Locate every blood parasite and identify its species.
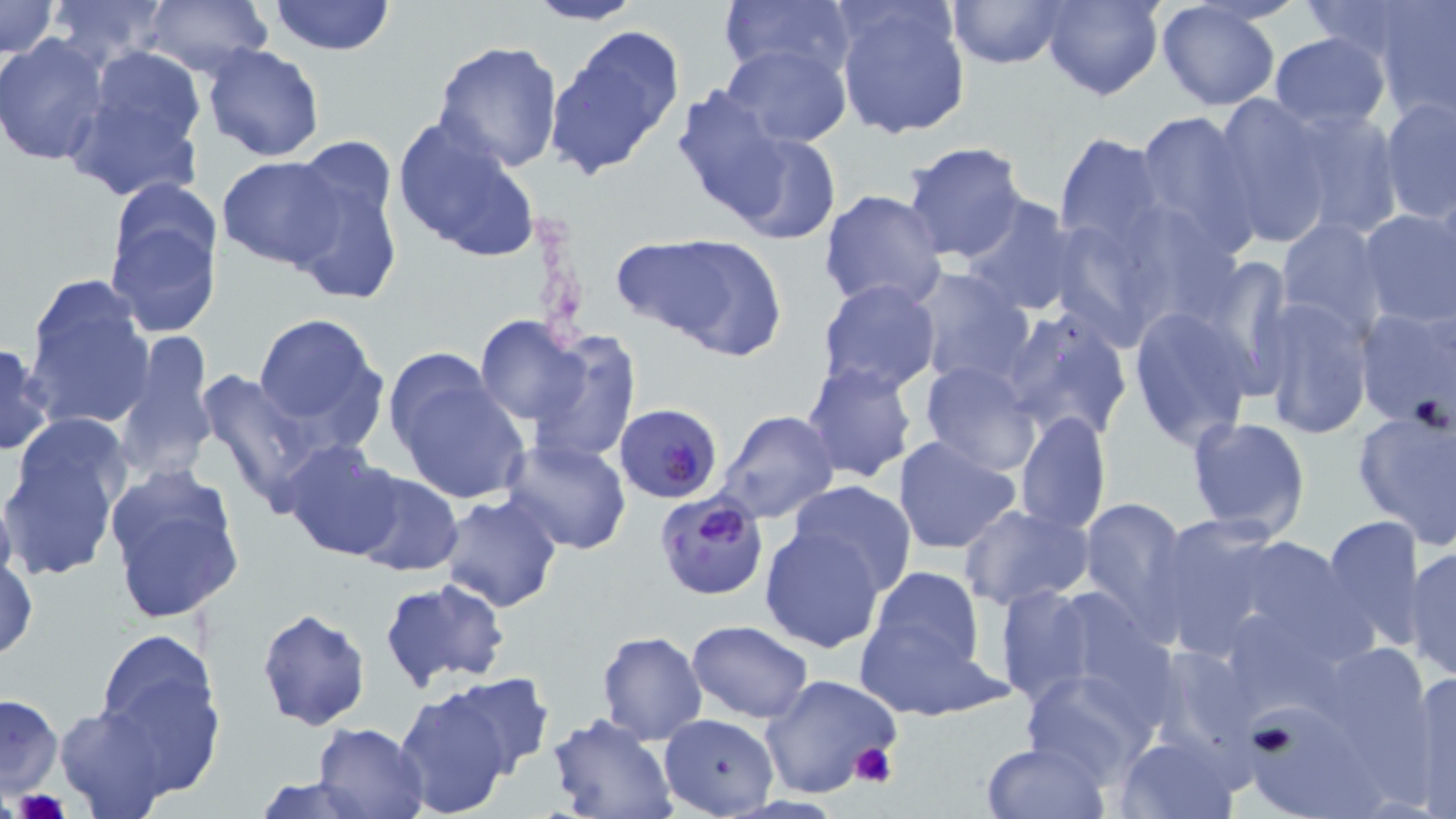
Approximate bounding boxes as (x1, y1, x2, y2) in pixels.
Plasmodium falciparum-infected red blood cells: (615, 403, 723, 503), (653, 491, 768, 600).
No Plasmodium ovale, Plasmodium malariae, Plasmodium vivax, Babesia divergens, or Trypanosoma brucei observed.

Platelet locations: (851, 743, 897, 788), (16, 790, 67, 819). Uninfected red blood cell locations: (0, 0, 59, 58), (41, 0, 176, 68), (142, 0, 273, 81), (267, 0, 397, 56), (525, 0, 642, 25), (718, 0, 856, 88), (946, 0, 1069, 69), (1042, 0, 1162, 101), (831, 1, 970, 141), (1156, 2, 1282, 111), (1374, 2, 1456, 122), (545, 23, 687, 181), (1268, 32, 1391, 131), (0, 35, 110, 166), (431, 40, 564, 172), (201, 43, 326, 163), (719, 43, 851, 147), (92, 46, 204, 152), (64, 70, 209, 203), (671, 88, 789, 220), (1208, 92, 1337, 250), (1378, 95, 1455, 223), (1280, 105, 1405, 240), (1133, 108, 1260, 257), (391, 116, 542, 265), (719, 126, 845, 246), (1054, 134, 1166, 250), (902, 140, 1030, 265), (281, 141, 404, 309), (217, 156, 347, 269), (103, 185, 223, 341), (819, 189, 947, 313), (957, 194, 1082, 318), (1358, 208, 1456, 329), (1275, 217, 1385, 337), (1063, 229, 1166, 359), (630, 233, 789, 360), (1215, 260, 1300, 399), (909, 269, 1033, 389), (22, 275, 157, 433), (817, 279, 942, 396), (1255, 296, 1373, 441), (1352, 305, 1456, 431), (997, 307, 1134, 444), (1128, 308, 1258, 450), (251, 312, 389, 448), (474, 316, 594, 429), (521, 331, 640, 466), (116, 332, 215, 482), (0, 341, 53, 455), (386, 354, 529, 505), (799, 361, 919, 485), (918, 361, 1042, 476), (194, 364, 331, 516), (746, 390, 890, 513), (1352, 400, 1456, 551), (715, 411, 839, 524), (1016, 411, 1111, 536), (1185, 415, 1311, 539), (893, 436, 1022, 557), (501, 439, 631, 554), (280, 440, 406, 561), (2, 442, 119, 581), (102, 463, 246, 626), (347, 471, 464, 577), (788, 479, 917, 596), (439, 493, 564, 613), (1075, 495, 1194, 636), (958, 503, 1095, 610), (1147, 513, 1288, 661), (1319, 514, 1429, 652), (758, 527, 886, 655), (1216, 533, 1379, 664), (1404, 546, 1455, 681), (0, 552, 37, 663), (865, 565, 987, 683), (377, 576, 511, 692), (990, 583, 1111, 708), (257, 607, 371, 732), (852, 610, 1003, 721), (687, 619, 813, 721), (89, 629, 226, 784), (595, 630, 708, 745), (1021, 665, 1162, 786), (1408, 669, 1456, 813), (435, 673, 555, 776), (761, 674, 902, 800), (394, 687, 519, 817), (1, 694, 64, 798), (1245, 703, 1389, 819), (55, 704, 176, 817), (659, 713, 777, 816), (544, 714, 680, 819), (314, 721, 430, 818), (1115, 733, 1241, 818), (981, 739, 1107, 819), (252, 775, 378, 817). Slide-level diagnosis: Plasmodium falciparum. Optical microscopy. May-Grünwald-Giemsa stain. Thin blood film. One field of a larger specimen. Image is 1456×819 pixels. Captured at 1000x magnification.